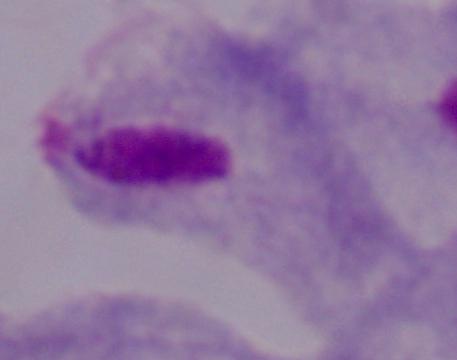
Summary:
  - Identification: trichomonad
  - Modality: photomicrograph
  - Magnification: 1000x